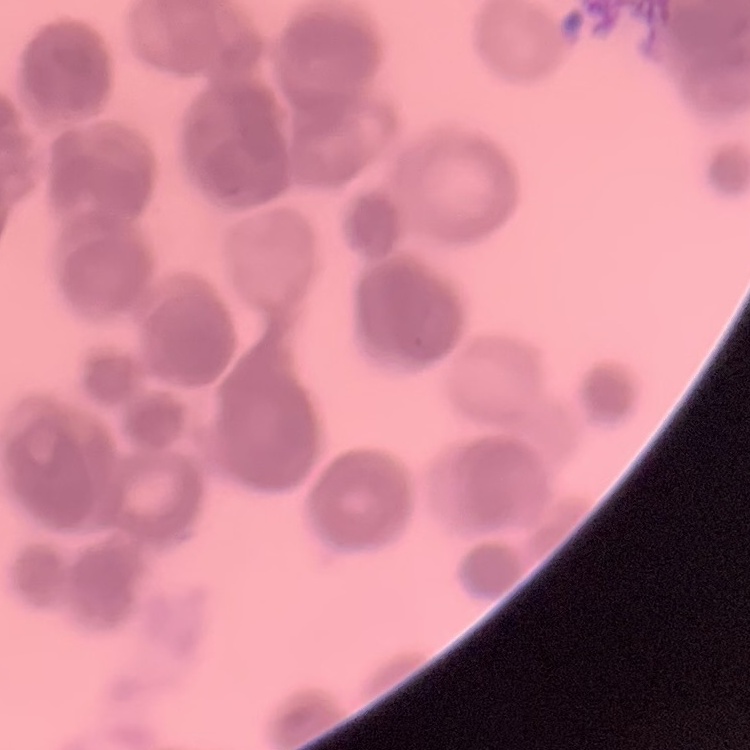
Summary:
  - Erythrocyte morphology: rouleaux formation
  - Image type: square crop of a larger photomicrograph
  - Preparation: thin blood film
  - Stain: Field's or Giemsa